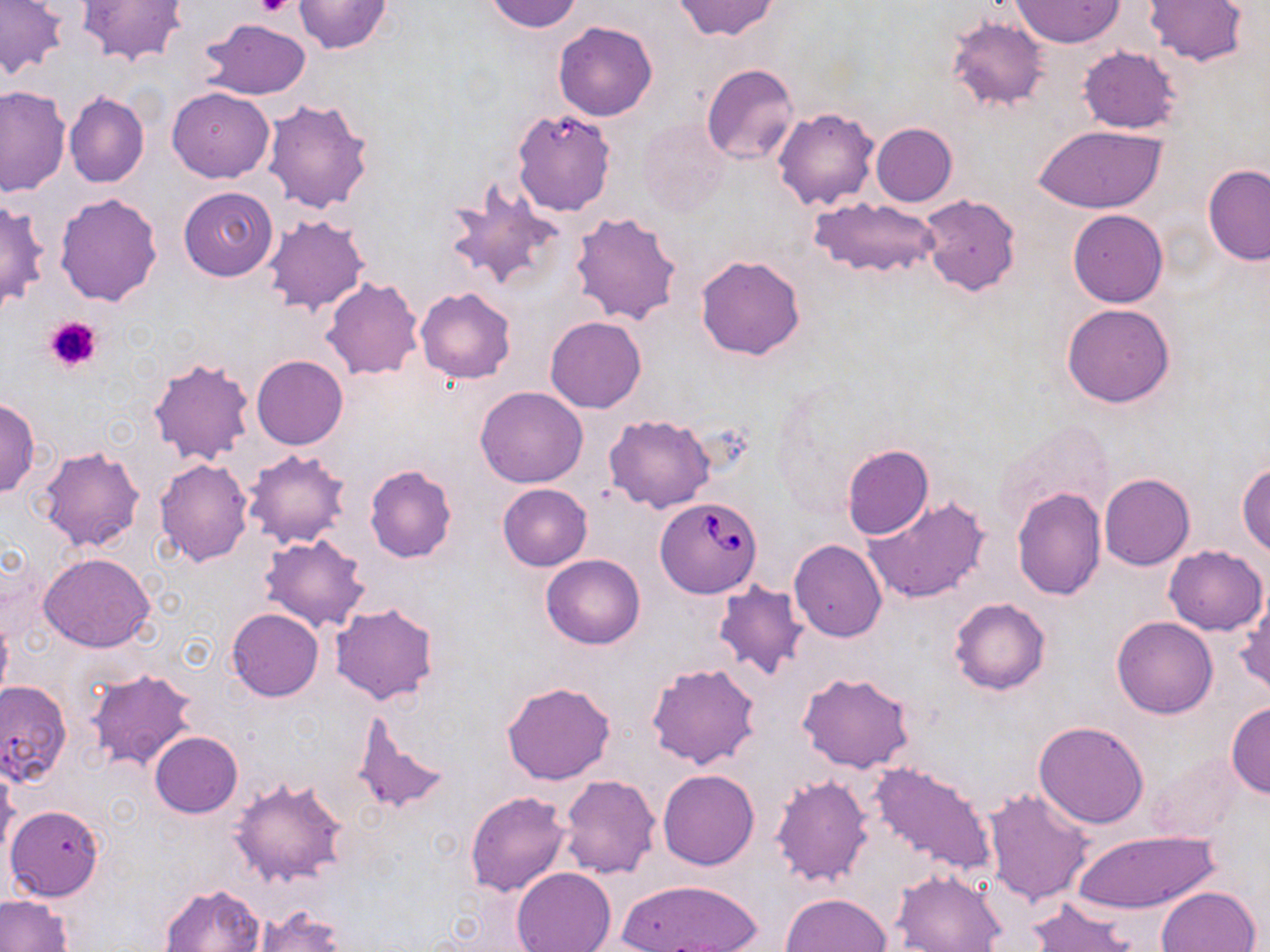
Approximate bounding boxes as (x1, y1, x2, y2) in pixels. Platelet locations: (256, 0, 294, 19), (43, 315, 102, 375). Babesia divergens-infected red blood cell locations: (511, 108, 617, 217), (655, 498, 762, 598). Uninfected red blood cell locations: (0, 0, 67, 79), (76, 0, 187, 66), (293, 0, 391, 53), (486, 0, 584, 33), (675, 0, 778, 40), (1009, 0, 1124, 47), (1144, 0, 1248, 66), (945, 16, 1049, 112), (199, 18, 313, 101), (554, 21, 658, 121), (1077, 46, 1183, 134), (701, 63, 798, 164), (0, 85, 71, 196), (166, 87, 275, 183), (64, 92, 149, 188), (261, 97, 373, 215), (771, 106, 879, 209), (638, 119, 728, 218), (870, 122, 958, 206), (1034, 125, 1166, 214), (1202, 164, 1270, 266), (445, 179, 560, 293), (178, 187, 279, 280), (53, 192, 163, 306), (918, 195, 1022, 297), (811, 196, 941, 280), (0, 197, 49, 315), (1068, 209, 1168, 307), (570, 211, 682, 325), (261, 214, 369, 317), (696, 254, 806, 360), (322, 276, 423, 380), (415, 287, 517, 383), (1061, 302, 1176, 408), (545, 315, 647, 414), (252, 355, 348, 450), (149, 356, 254, 466), (475, 387, 588, 489), (0, 398, 42, 497), (604, 414, 716, 513), (994, 422, 1114, 535), (842, 445, 933, 540), (38, 446, 145, 554), (241, 450, 351, 550), (153, 458, 253, 566), (1237, 461, 1270, 557), (364, 465, 457, 562), (1099, 472, 1194, 569), (498, 483, 591, 571), (1011, 486, 1106, 601), (864, 495, 992, 604), (258, 533, 370, 633), (789, 539, 887, 643), (1164, 546, 1267, 635), (39, 552, 156, 652), (541, 554, 644, 648), (712, 579, 810, 681), (1236, 592, 1270, 696), (949, 596, 1052, 695), (330, 602, 441, 706), (227, 608, 323, 701), (1112, 616, 1218, 719), (646, 662, 762, 771), (86, 667, 198, 771), (797, 672, 917, 774), (1, 680, 71, 784), (501, 680, 615, 786), (1226, 702, 1270, 798), (354, 711, 448, 817), (1033, 720, 1149, 828), (149, 732, 242, 817), (1143, 749, 1250, 845), (867, 761, 998, 880), (0, 762, 20, 857), (658, 768, 759, 870), (769, 773, 874, 888), (560, 774, 661, 879), (229, 776, 353, 888), (983, 787, 1097, 909), (465, 791, 571, 896), (6, 804, 104, 901), (1070, 828, 1221, 914), (513, 867, 617, 952), (890, 870, 1005, 952), (614, 878, 764, 952), (161, 883, 265, 951), (1155, 885, 1261, 952), (780, 893, 891, 952), (0, 894, 71, 952), (1027, 898, 1141, 952), (252, 905, 345, 952). Slide-level diagnosis: Babesia divergens. Light microscopy. May-Grünwald-Giemsa stain. Thin blood film. Captured at 1000x magnification. One field of a larger specimen. Image is 1270×952 pixels.